Outline each blood parasite and name the species.
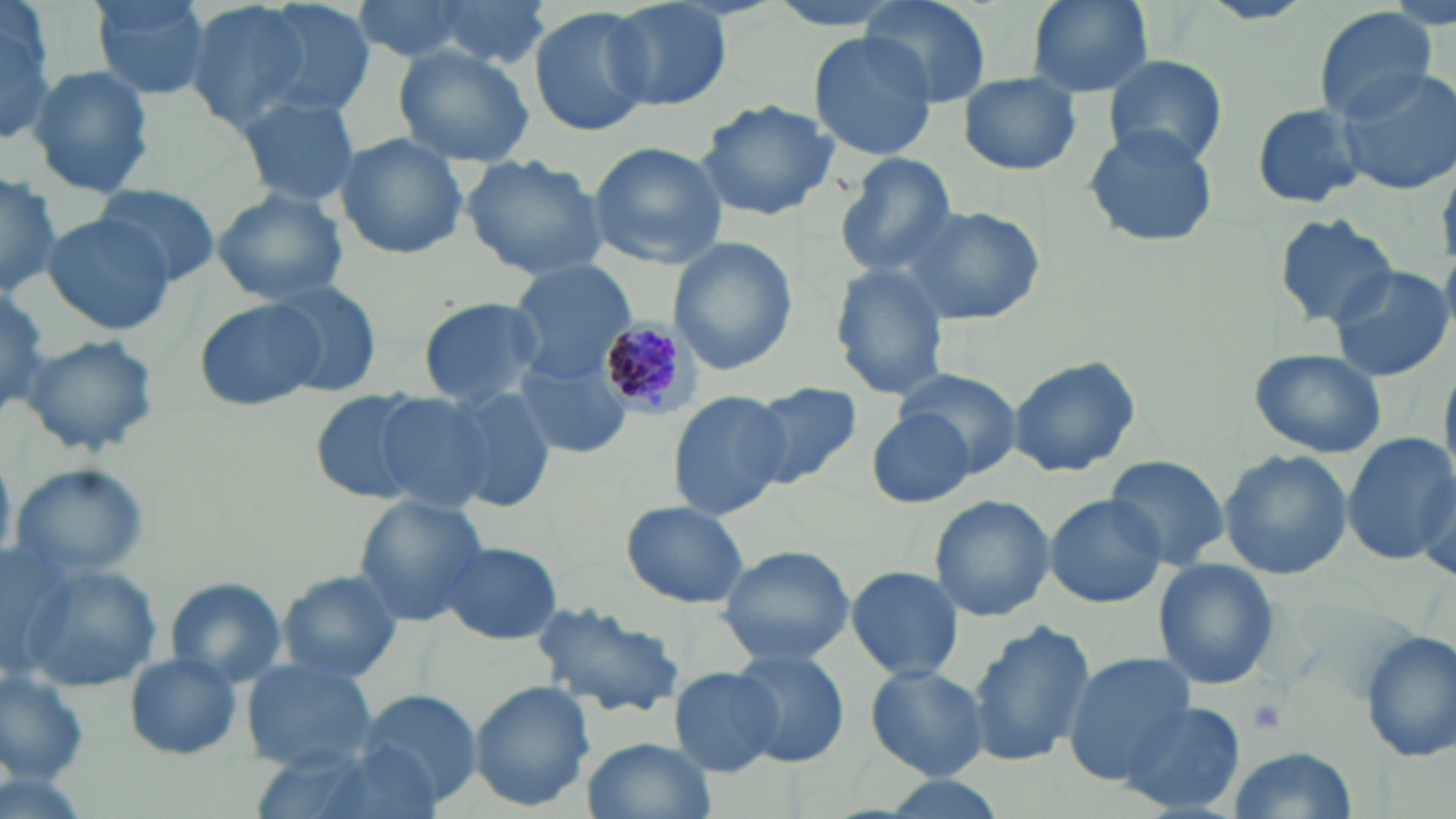

Approximate bounding boxes as (x1, y1, x2, y2) in pixels.
Plasmodium malariae-infected red blood cells: (597, 317, 710, 417).
No Plasmodium falciparum, Plasmodium ovale, Plasmodium vivax, Babesia divergens, or Trypanosoma brucei observed.

slide-level diagnosis = Plasmodium malariae
image size = 1456×819 pixels
modality = optical microscopy
preparation = thin blood film
uninfected red blood cell locations = approximate bounding boxes as (x1, y1, x2, y2) in pixels: (89, 0, 214, 103), (240, 0, 378, 123), (352, 0, 502, 63), (424, 0, 552, 68), (603, 0, 733, 113), (861, 0, 993, 109), (1024, 0, 1155, 98), (181, 1, 322, 136), (0, 2, 57, 142), (529, 6, 656, 138), (1313, 8, 1437, 123), (809, 30, 937, 161), (392, 43, 539, 169), (1101, 53, 1229, 168), (28, 64, 155, 199), (1337, 67, 1456, 195), (958, 72, 1082, 177), (234, 92, 362, 207), (695, 98, 842, 220), (1249, 102, 1370, 208), (1083, 125, 1220, 249), (333, 132, 469, 259), (587, 141, 729, 268), (462, 152, 613, 283), (832, 154, 958, 280), (0, 168, 63, 293), (93, 184, 220, 283), (211, 188, 350, 305), (895, 202, 1045, 326), (1274, 211, 1396, 325), (40, 212, 174, 336), (667, 237, 799, 376), (506, 260, 633, 382), (1327, 264, 1454, 383), (828, 265, 951, 399), (0, 277, 51, 419), (261, 279, 382, 390), (193, 295, 331, 413), (420, 296, 549, 407), (22, 333, 158, 458), (1246, 346, 1387, 458), (516, 352, 635, 459), (1007, 355, 1140, 478), (896, 367, 1024, 477), (746, 381, 862, 489), (666, 387, 791, 519), (310, 389, 435, 505), (436, 389, 555, 511), (370, 391, 508, 513), (869, 407, 977, 509), (1344, 432, 1454, 566), (1217, 450, 1354, 578), (1102, 454, 1231, 570), (11, 463, 154, 581), (1042, 493, 1170, 609), (929, 494, 1055, 621), (351, 495, 491, 626), (622, 502, 750, 609), (437, 541, 563, 645), (717, 544, 855, 666), (1152, 558, 1283, 690), (16, 561, 164, 696), (844, 565, 966, 682), (274, 570, 404, 685), (164, 577, 287, 689), (529, 599, 685, 721), (966, 620, 1096, 767), (1358, 630, 1456, 764), (728, 649, 849, 766), (1060, 652, 1197, 786), (121, 653, 243, 760), (241, 659, 378, 773), (865, 664, 990, 781), (0, 667, 91, 786), (668, 668, 783, 776), (469, 681, 596, 812), (359, 691, 481, 805), (1119, 699, 1247, 814), (583, 736, 716, 819), (1222, 747, 1361, 818), (864, 774, 1016, 819)
magnification = 1000x
platelet locations = approximate bounding boxes as (x1, y1, x2, y2) in pixels: (1246, 697, 1288, 735)
stain = May-Grünwald-Giemsa
field of view = single